Assess the morphology of the red blood cells.
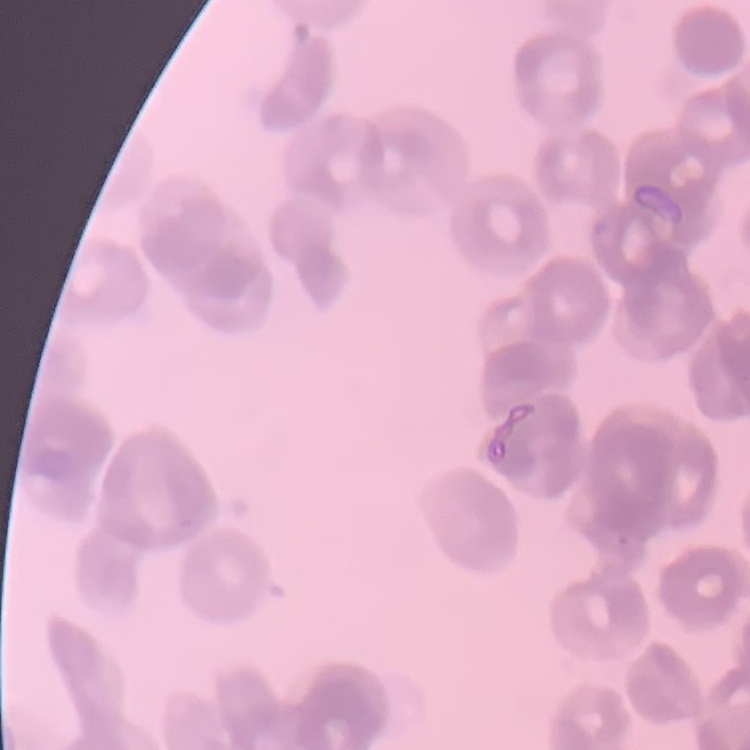
Rouleaux formation.

Summary:
  - Image type: one tile cut from a larger photomicrograph
  - Stain: Field's or Giemsa
  - Preparation: thin blood smear